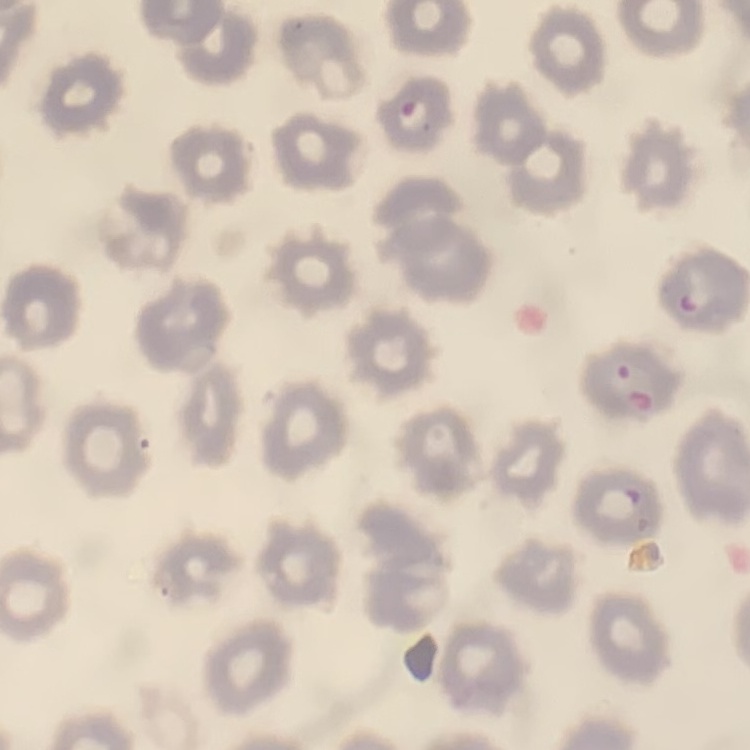
red_blood_cell_morphology: no rouleaux formation
preparation: thin blood film
image_type: one tile cut from a larger photomicrograph
stain: Field's or Giemsa